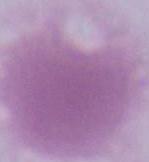 1000x magnification. Micrograph. An erythrocyte is seen.